Report the malaria status.
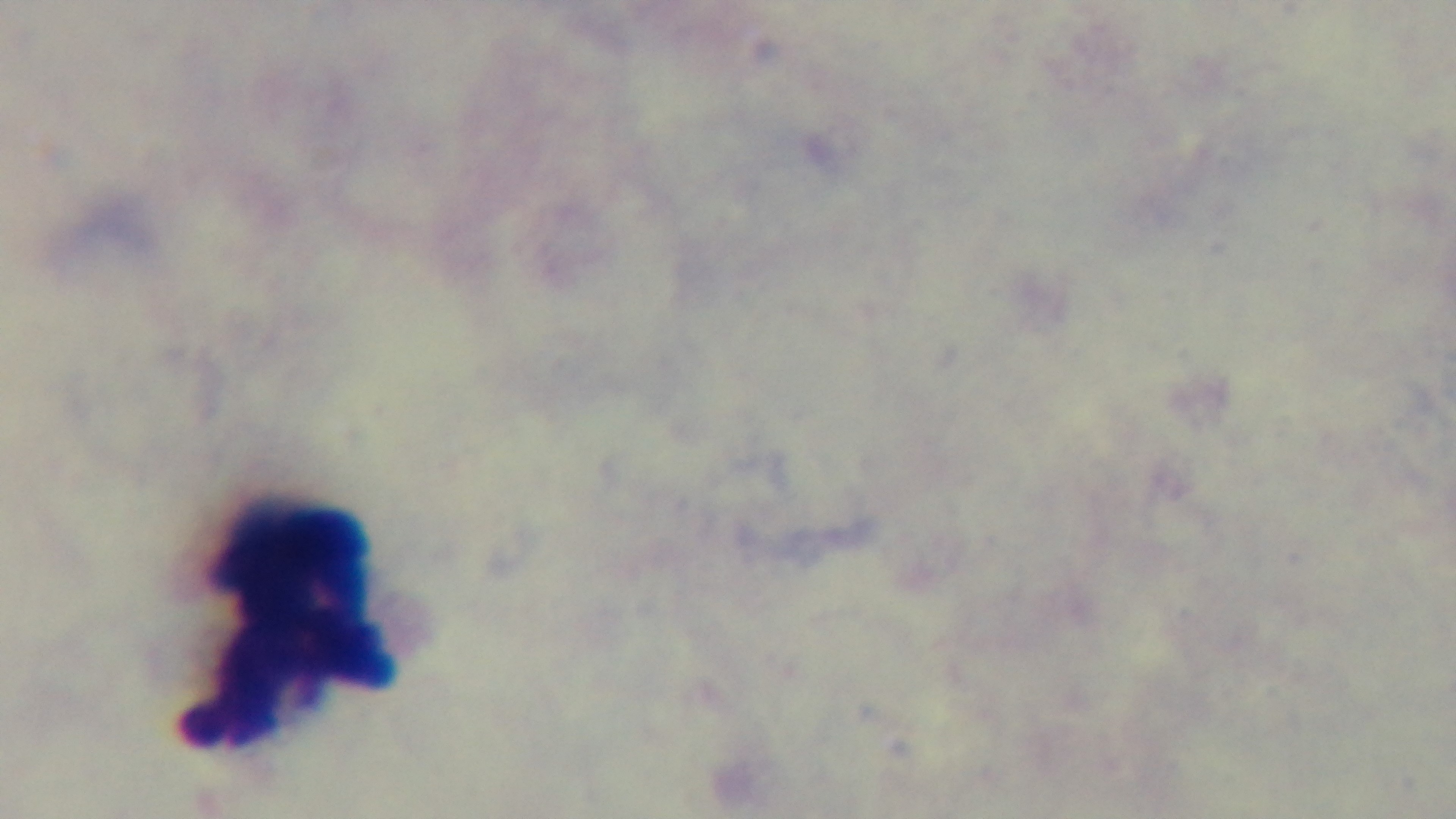
It is uninfected.

modality = light microscopy
objective = 100x oil immersion
capture = mounted 4K digital camera
stain = Giemsa
field of view = one from the slide
preparation = thick blood film